Report the malaria status of this cell.
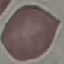

Uninfected.

Summary:
  - Preparation: thin smear
  - Capture: smartphone camera at the microscope eyepiece
  - Image type: automatically extracted cell patch, resized to 64 × 64 pixels
  - Stain: Giemsa